State the blood parasite species.
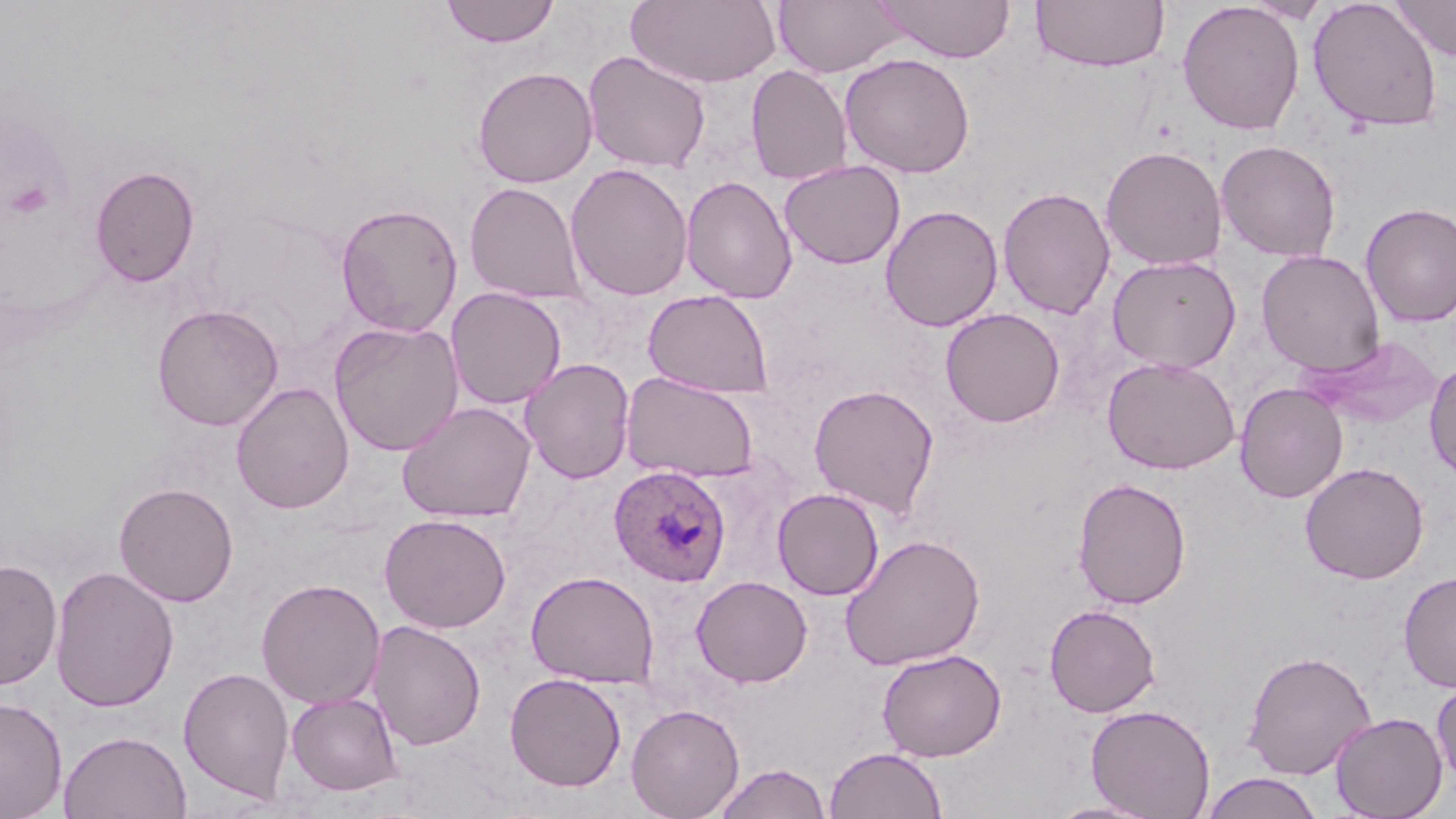
Plasmodium ovale.

Summary:
  - Coordinate format: approximate bounding boxes as [x1, y1, x2, y2] in pixels
  - Plasmodium ovale-infected red blood cell locations: [608, 465, 731, 587]
  - Platelet locations: [5, 179, 54, 219]
  - Uninfected red blood cell locations: [440, 0, 560, 48], [626, 0, 782, 88], [790, 0, 926, 139], [873, 0, 1016, 63], [1031, 0, 1170, 72], [1244, 0, 1332, 23], [1308, 0, 1443, 133], [1390, 0, 1456, 61], [772, 1, 906, 77], [1176, 1, 1305, 135], [583, 50, 711, 173], [839, 52, 976, 178], [746, 64, 853, 185], [472, 66, 598, 188], [1216, 140, 1341, 262], [1100, 145, 1228, 270], [778, 159, 905, 269], [565, 163, 694, 301], [89, 164, 200, 288], [681, 175, 798, 304], [465, 182, 586, 304], [997, 186, 1116, 320], [335, 202, 463, 337], [1360, 202, 1456, 328], [880, 204, 1003, 331], [1256, 250, 1385, 376], [1107, 255, 1241, 373], [446, 287, 566, 409], [643, 289, 774, 398], [151, 303, 285, 431], [940, 307, 1065, 428], [329, 320, 464, 456], [1305, 335, 1444, 429], [1101, 356, 1240, 474], [519, 358, 636, 484], [1424, 359, 1456, 482], [620, 371, 759, 483], [231, 382, 354, 514], [1234, 382, 1348, 503], [808, 383, 940, 519], [397, 401, 536, 523], [1299, 461, 1430, 584], [1072, 476, 1192, 609], [114, 481, 239, 607], [772, 487, 885, 600], [379, 513, 511, 633], [840, 534, 986, 671], [0, 558, 62, 691], [49, 565, 180, 713], [525, 570, 659, 688], [1398, 571, 1456, 693], [691, 575, 812, 688], [256, 578, 385, 710], [1044, 603, 1161, 717], [368, 619, 487, 750], [876, 648, 1007, 761], [1241, 649, 1377, 780], [178, 666, 294, 803], [504, 672, 627, 791], [1431, 679, 1456, 787], [285, 692, 404, 796], [0, 696, 68, 818], [626, 703, 745, 819], [1085, 703, 1216, 818], [1330, 711, 1448, 818], [59, 729, 192, 819], [824, 746, 947, 819], [713, 762, 831, 819], [1200, 772, 1325, 819], [1043, 798, 1164, 818]
  - Stain: May-Grünwald-Giemsa
  - Preparation: thin blood smear
  - Modality: optical microscopy
  - Field of view: single
  - Image size: 1456×819 pixels
  - Magnification: 1000x